State which parasite is depicted.
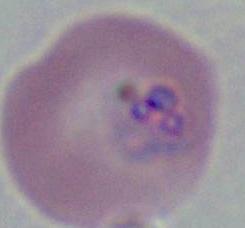
Plasmodium.

Photomicrograph. 400x or 1000x magnification.